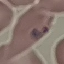

Malaria status: parasitized. Thin smear of blood. Photographed with a smartphone camera at the microscope eyepiece. Giemsa-stained preparation. Cell patch, automatically extracted from a larger field of view and resized to 64 × 64 pixels.